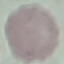 Malaria status: uninfected. Photographed with a smartphone camera at the microscope eyepiece. Giemsa stain. Automatically extracted cell patch, resized to 64 × 64 pixels. Thin blood film.